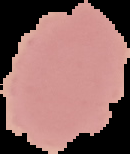

Result: no malaria parasites seen. Segmented cell region on a black background. From a thin blood film. Image is 130×154 pixels.